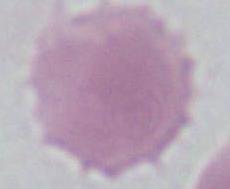
Summary:
  - Modality: micrograph
  - Identification: erythrocyte
  - Magnification: 1000x